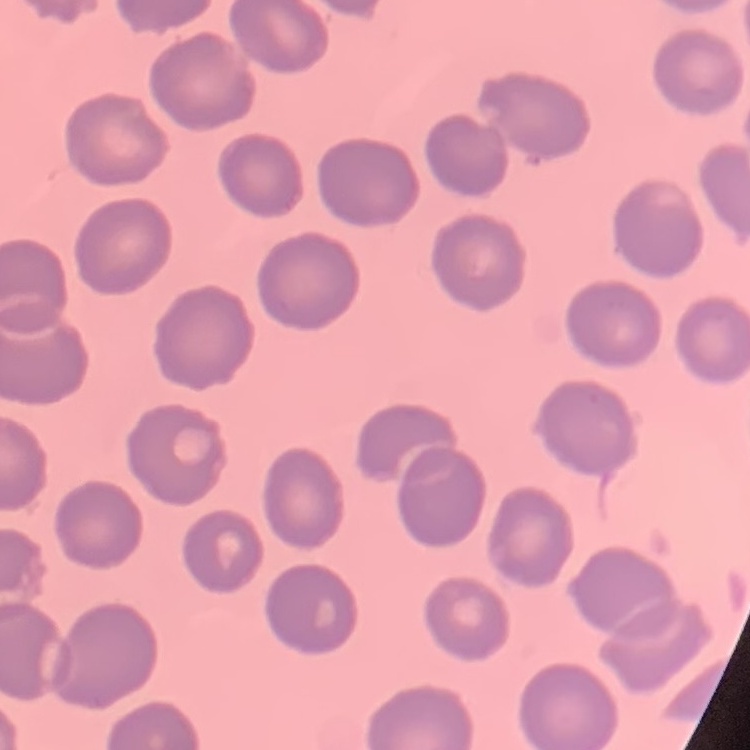

The red blood cells show no rouleaux formation. One tile cut from a larger photomicrograph. Thin blood smear. Stained with either Field's or Giemsa.